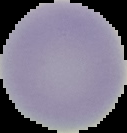

Summary:
  - Image size: 127×133 pixels
  - Malaria status: uninfected
  - Image type: segmented cell region on a black background
  - Preparation: thin blood smear